Describe the morphology of the erythrocytes.
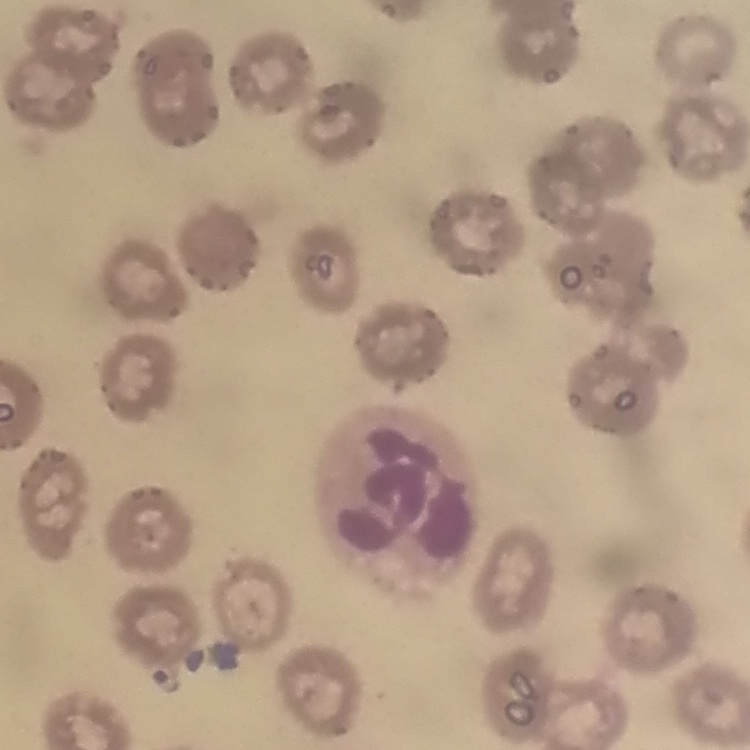
They show no rouleaux formation.

preparation = thin peripheral smear
image type = square crop of a larger photomicrograph
stain = Field's or Giemsa